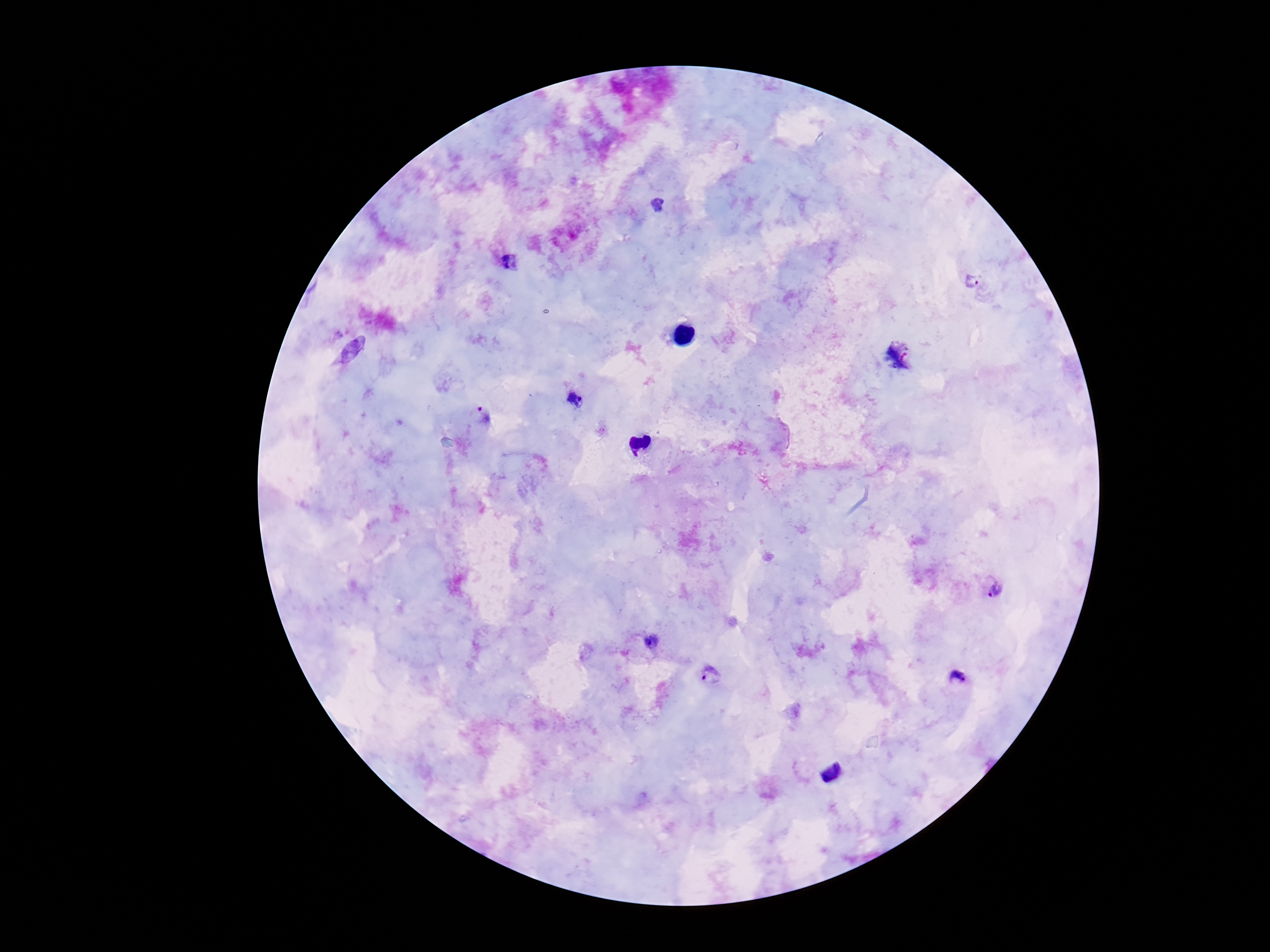
capture = smartphone camera through the microscope eyepiece
patient malaria status = positive
magnification = 100x
preparation = thick blood film
Plasmodium parasite locations = approximate centers as [x, y] in pixels: [510, 263], [972, 281], [898, 357], [574, 400], [481, 419], [996, 592], [651, 641], [711, 673], [958, 678]
stain = Giemsa
field of view = single
image size = 1270×952 pixels